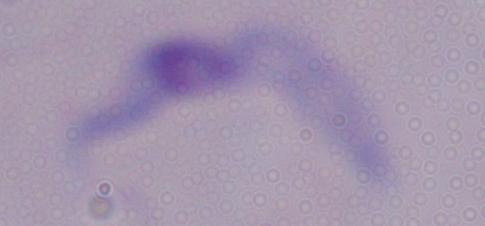
Summary:
  - Identification: trypanosome
  - Modality: photomicrograph
  - Magnification: 1000x